State the blood parasite species.
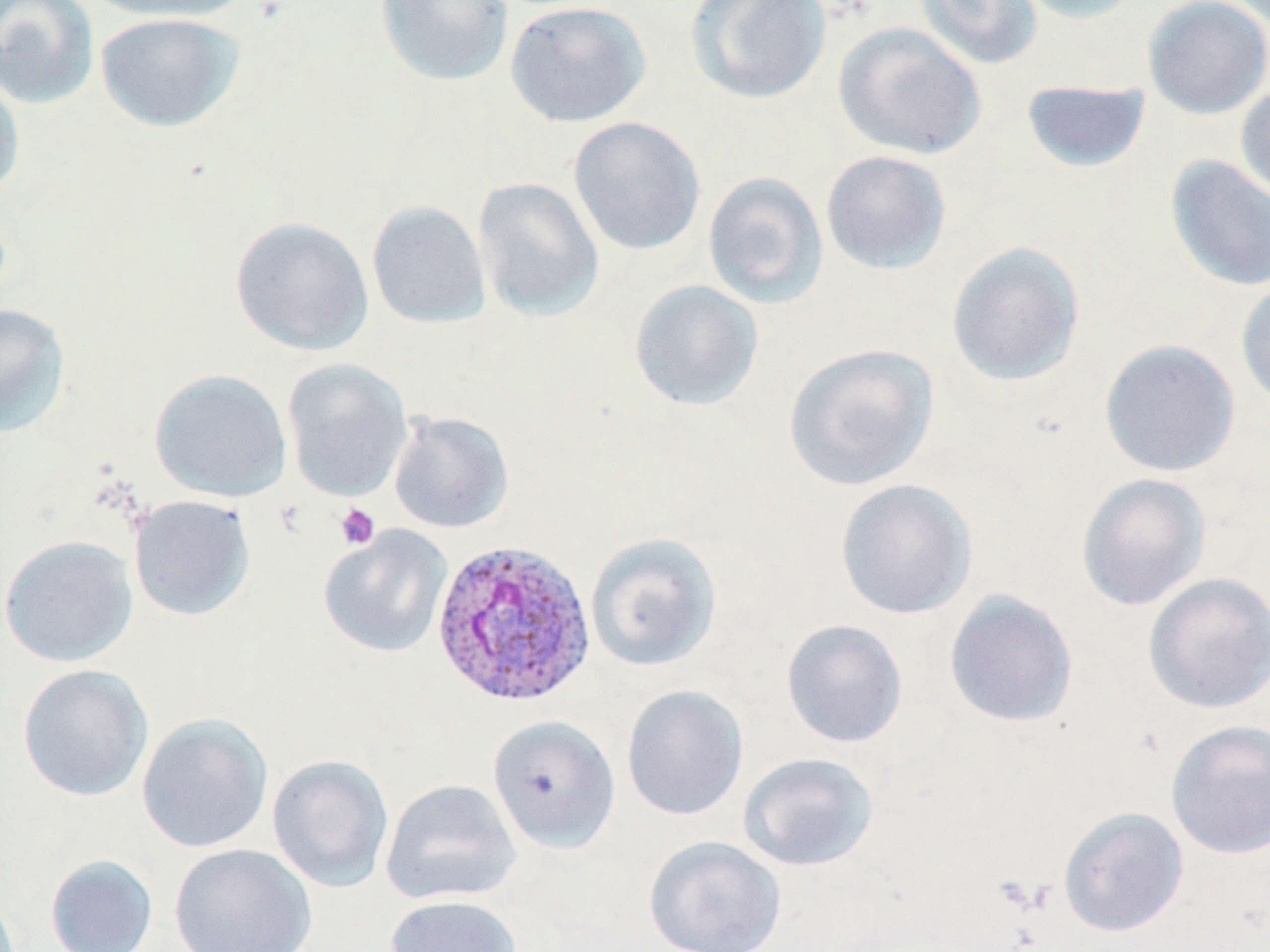
Plasmodium ovale.

field_of_view: single
stain: May-Grünwald-Giemsa
image_size: 1270×952 pixels
plasmodium_ovale_infected_red_blood_cell_locations: 'approximate bounding boxes as [x1, y1, x2, y2] in pixels: [430, 539, 595, 708]'
platelet_locations: 'approximate bounding boxes as [x1, y1, x2, y2] in pixels: [334, 503, 381, 550]'
preparation: thin blood film
uninfected_red_blood_cell_locations: 'approximate bounding boxes as [x1, y1, x2, y2] in pixels: [0, 0, 100, 109], [82, 0, 252, 23], [376, 0, 514, 87], [684, 0, 832, 105], [914, 0, 1043, 70], [1012, 0, 1143, 24], [1142, 0, 1270, 120], [505, 1, 651, 128], [95, 12, 244, 132], [833, 22, 987, 160], [0, 69, 26, 199], [1021, 80, 1151, 173], [1235, 82, 1270, 204], [568, 116, 706, 256], [821, 150, 952, 275], [1164, 154, 1270, 292], [703, 172, 828, 308], [473, 178, 605, 321], [366, 200, 491, 329], [230, 216, 374, 356], [946, 241, 1086, 387], [1236, 278, 1270, 413], [629, 279, 764, 411], [0, 304, 70, 440], [1099, 339, 1241, 478], [783, 342, 939, 492], [282, 359, 413, 502], [150, 369, 292, 502], [388, 410, 514, 534], [1076, 473, 1212, 610], [834, 479, 977, 620], [129, 494, 256, 621], [319, 526, 453, 658], [585, 532, 722, 671], [0, 535, 138, 667], [1143, 572, 1270, 714], [944, 590, 1079, 728], [780, 619, 908, 748], [17, 664, 154, 801], [622, 685, 748, 820], [136, 712, 274, 853], [488, 715, 621, 854], [1165, 719, 1270, 859], [737, 752, 880, 872], [267, 754, 394, 892], [380, 778, 521, 906], [1058, 806, 1189, 937], [643, 835, 787, 952], [169, 843, 317, 952], [45, 853, 158, 952], [384, 894, 523, 952]'
magnification: 1000x
modality: light microscopy